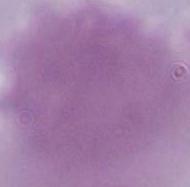

magnification: 1000x
modality: micrograph
identification: red blood cell